Outline each blood parasite and name the species.
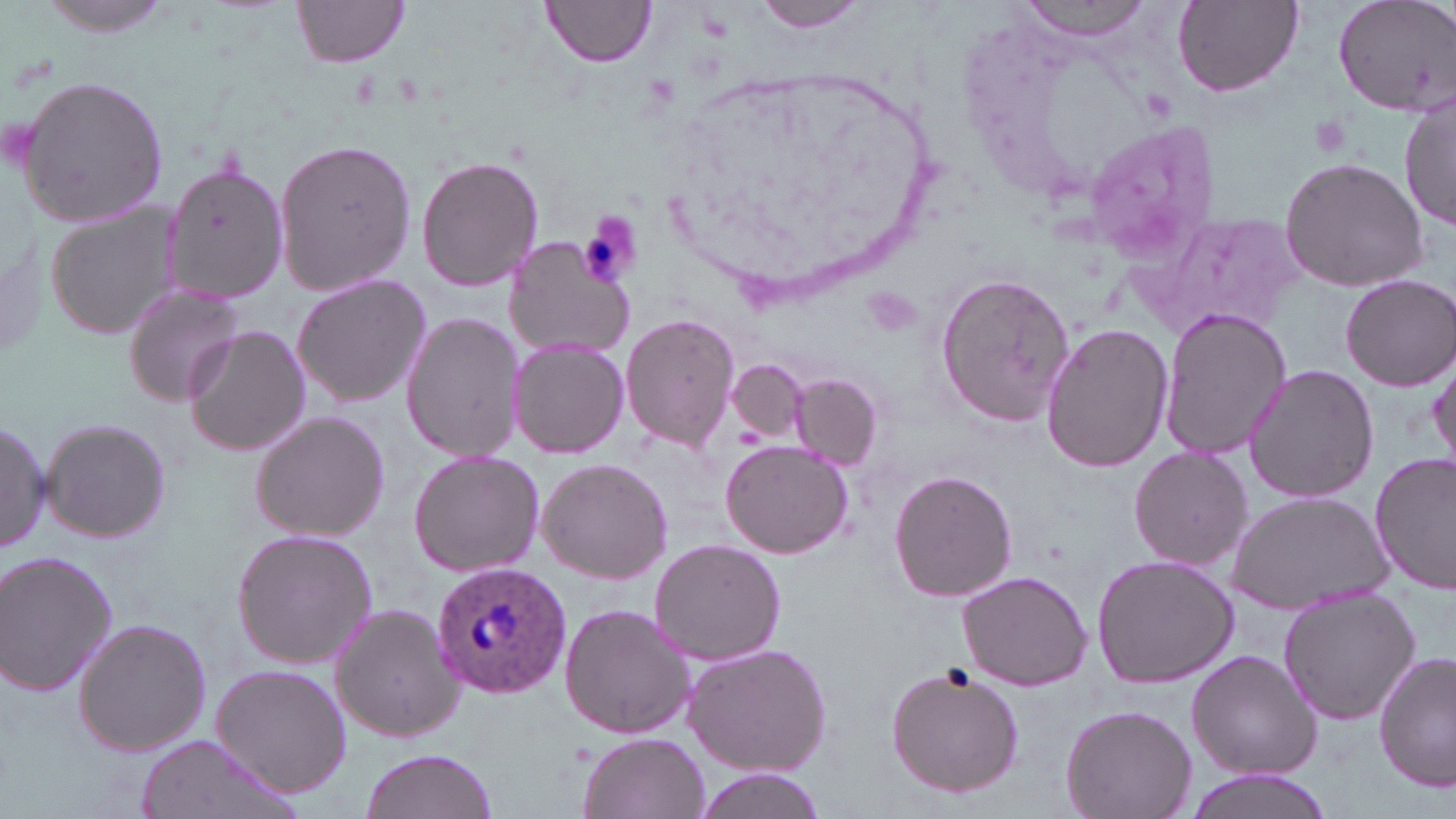

Approximate bounding boxes as (x1, y1, x2, y2) in pixels.
Plasmodium ovale-infected red blood cells: (431, 559, 569, 697).
No Plasmodium falciparum, Plasmodium malariae, Plasmodium vivax, Babesia divergens, or Trypanosoma brucei observed.

slide_level_diagnosis: Plasmodium ovale
platelet_locations: 'approximate bounding boxes as (x1, y1, x2, y2) in pixels: (1308, 111, 1356, 159), (577, 214, 642, 289)'
uninfected_red_blood_cell_locations: 'approximate bounding boxes as (x1, y1, x2, y2) in pixels: (31, 0, 184, 36), (292, 0, 412, 69), (754, 0, 876, 35), (1015, 0, 1158, 41), (1171, 0, 1302, 98), (1331, 0, 1456, 116), (542, 1, 655, 69), (15, 74, 171, 227), (1400, 91, 1455, 238), (1081, 119, 1219, 260), (272, 138, 416, 298), (417, 155, 544, 291), (1279, 156, 1431, 289), (162, 159, 287, 307), (45, 204, 184, 341), (1139, 213, 1304, 339), (502, 235, 634, 359), (290, 272, 431, 408), (936, 272, 1075, 426), (1338, 272, 1456, 389), (121, 280, 250, 407), (1158, 307, 1289, 462), (401, 311, 525, 462), (620, 314, 741, 452), (1040, 322, 1174, 474), (183, 324, 309, 457), (508, 335, 630, 460), (1430, 348, 1456, 471), (727, 359, 807, 443), (1242, 364, 1380, 503), (792, 373, 881, 469), (248, 410, 390, 543), (0, 416, 50, 558), (40, 416, 170, 543), (721, 440, 853, 559), (1128, 445, 1254, 570), (408, 450, 545, 578), (1371, 454, 1456, 593), (536, 457, 673, 583), (888, 469, 1018, 603), (1228, 491, 1395, 612), (231, 528, 378, 669), (648, 538, 786, 667), (0, 549, 119, 697), (1090, 554, 1241, 688), (957, 569, 1095, 690), (1277, 590, 1423, 725), (329, 602, 466, 742), (559, 604, 697, 739), (72, 618, 212, 757), (684, 641, 834, 777), (1186, 649, 1321, 780), (1375, 651, 1455, 793), (211, 662, 354, 798), (884, 662, 1027, 798), (1060, 704, 1196, 819), (577, 731, 708, 819), (131, 734, 303, 819), (359, 748, 497, 819), (689, 768, 823, 818), (1177, 768, 1341, 819)'
modality: light microscopy
field_of_view: one of a larger specimen
magnification: 1000x
stain: May-Grünwald-Giemsa
image_size: 1456×819 pixels
preparation: thin blood film